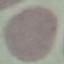 Result: negative for malaria parasites. Acquired by smartphone through the microscope eyepiece. Giemsa stain. Thin blood smear. Automatically extracted cell patch, resized to 64 × 64 pixels.